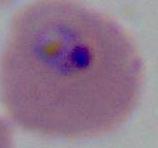
A Plasmodium parasite is shown. Photomicrograph. 400x or 1000x magnification.